Give a bounding box for every trophozoite.
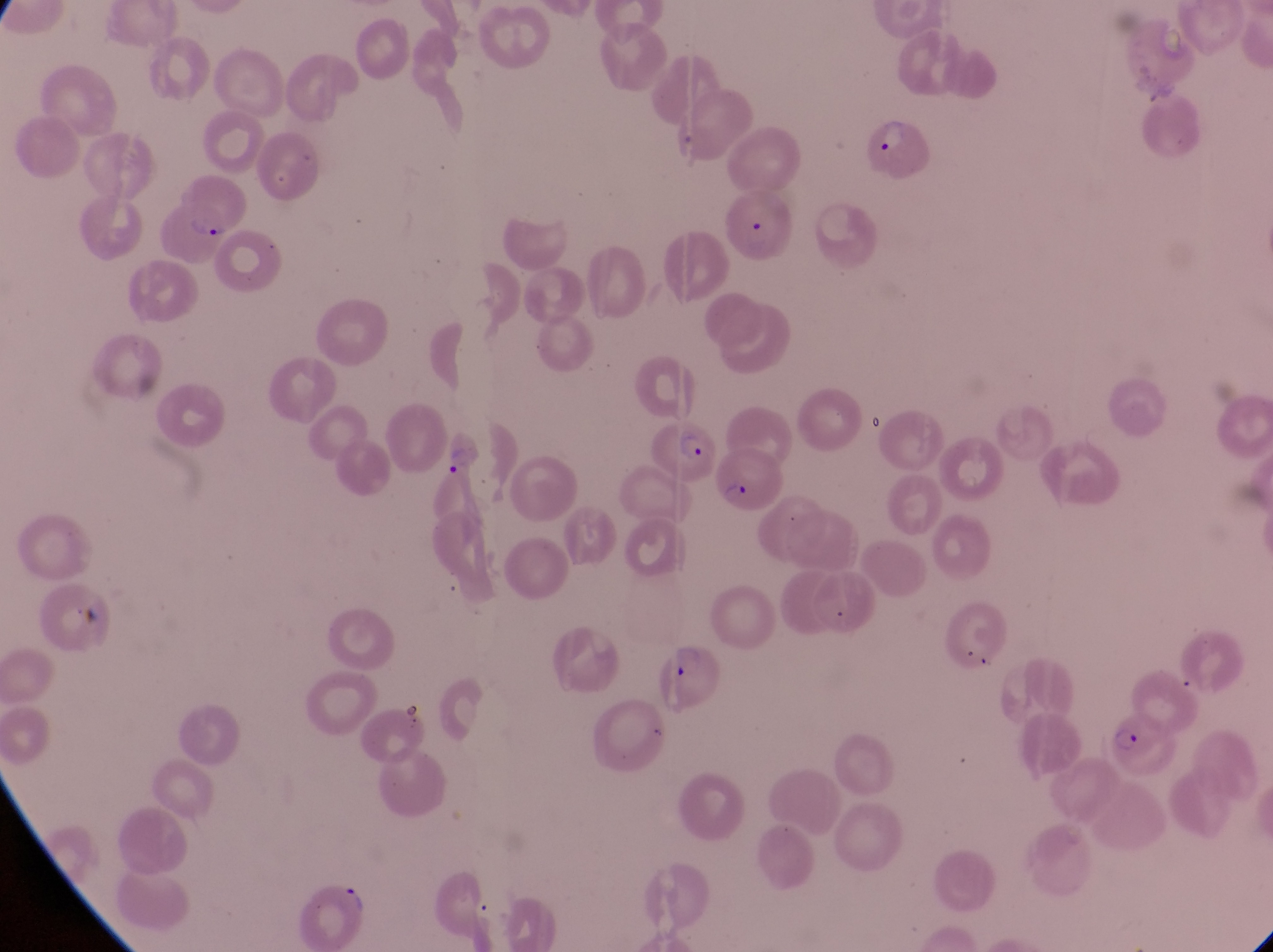

Approximate bounding boxes as {left, top, right, bottom} in pixels.
Trophozoites: {442, 447, 479, 482}.

Parasitised red blood cell locations: {863, 120, 940, 185}, {721, 193, 798, 261}, {165, 200, 239, 268}, {654, 415, 717, 483}, {717, 449, 787, 517}, {651, 642, 726, 716}, {1103, 719, 1178, 782}. Artifact (platelet-like body, stain precipitate, or debris) locations: {69, 610, 101, 637}. Captured by a smartphone held over the eyepiece of an Olympus CX-23 microscope. Magnification of 1000x. Thin blood smear. Single field of view. Sample from Uganda. Image is 1273×952 pixels.